Locate every blood parasite and identify its species.
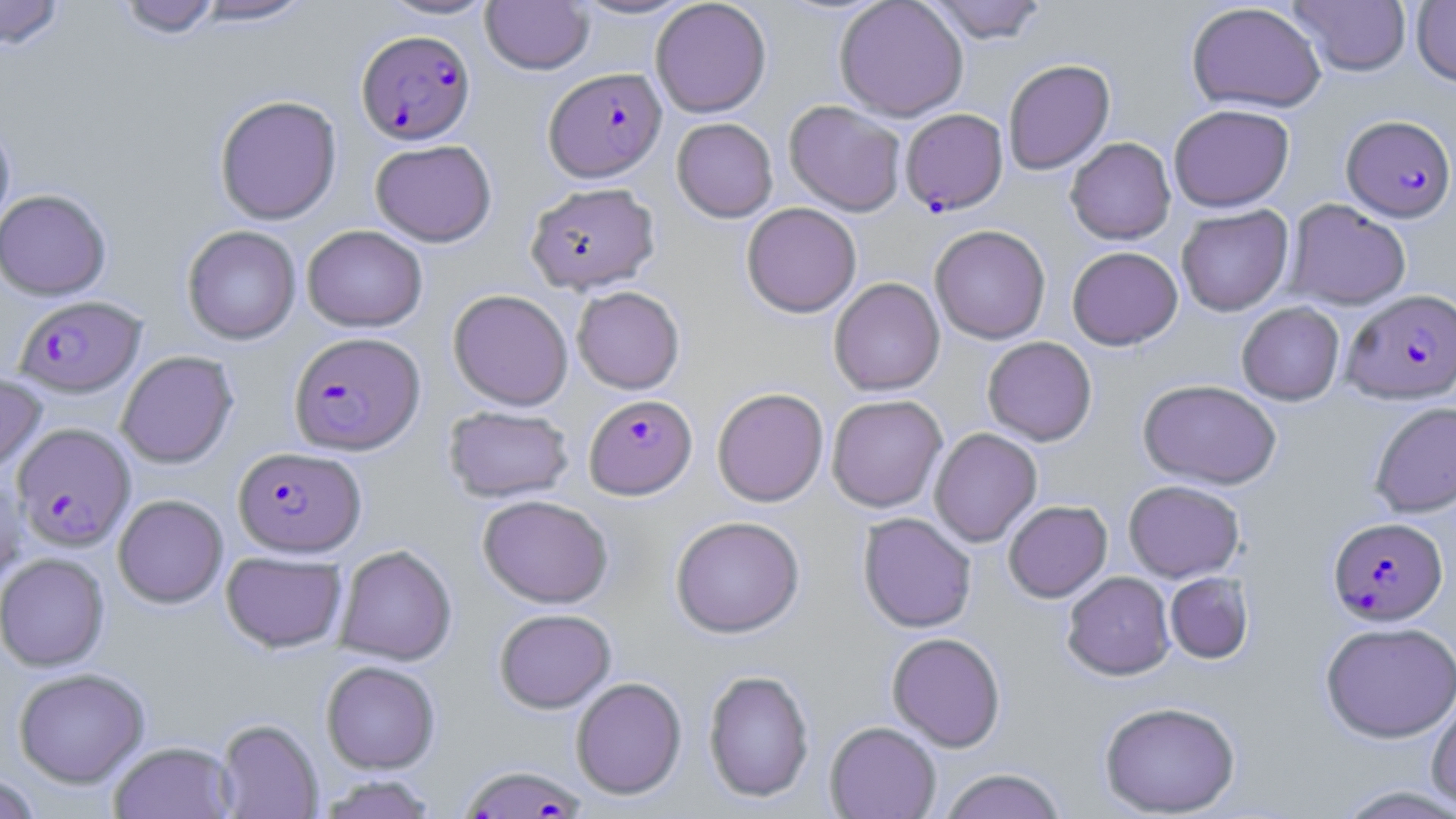
Approximate bounding boxes as named x1/y1/x2/y2 corners in pixels.
Plasmodium falciparum-infected red blood cells: (x1=356, y1=29, x2=475, y2=144), (x1=544, y1=66, x2=667, y2=182), (x1=900, y1=108, x2=1008, y2=214), (x1=1342, y1=115, x2=1455, y2=222), (x1=1342, y1=289, x2=1456, y2=404), (x1=14, y1=295, x2=146, y2=397), (x1=289, y1=331, x2=425, y2=455), (x1=584, y1=394, x2=697, y2=499), (x1=13, y1=423, x2=135, y2=551), (x1=233, y1=446, x2=366, y2=557), (x1=1328, y1=517, x2=1448, y2=625), (x1=458, y1=764, x2=587, y2=819).
No Plasmodium ovale, Plasmodium malariae, Plasmodium vivax, Babesia divergens, or Trypanosoma brucei observed.

Uninfected red blood cell locations: (x1=0, y1=0, x2=65, y2=50), (x1=115, y1=0, x2=222, y2=39), (x1=188, y1=0, x2=315, y2=26), (x1=377, y1=0, x2=499, y2=20), (x1=567, y1=0, x2=698, y2=20), (x1=650, y1=0, x2=772, y2=118), (x1=834, y1=0, x2=969, y2=121), (x1=923, y1=0, x2=1049, y2=43), (x1=1288, y1=0, x2=1412, y2=76), (x1=1411, y1=0, x2=1456, y2=87), (x1=481, y1=1, x2=594, y2=75), (x1=1186, y1=2, x2=1326, y2=114), (x1=1003, y1=58, x2=1115, y2=175), (x1=214, y1=95, x2=342, y2=225), (x1=783, y1=100, x2=906, y2=216), (x1=1168, y1=104, x2=1294, y2=212), (x1=672, y1=117, x2=778, y2=222), (x1=0, y1=121, x2=15, y2=235), (x1=1065, y1=137, x2=1176, y2=244), (x1=370, y1=139, x2=497, y2=247), (x1=525, y1=182, x2=661, y2=293), (x1=0, y1=189, x2=111, y2=300), (x1=1284, y1=199, x2=1411, y2=311), (x1=741, y1=202, x2=862, y2=318), (x1=1176, y1=205, x2=1293, y2=316), (x1=302, y1=225, x2=427, y2=332), (x1=929, y1=225, x2=1051, y2=344), (x1=182, y1=226, x2=301, y2=344), (x1=1067, y1=246, x2=1183, y2=350), (x1=829, y1=278, x2=945, y2=396), (x1=572, y1=286, x2=685, y2=394), (x1=448, y1=289, x2=573, y2=411), (x1=1236, y1=302, x2=1345, y2=405), (x1=982, y1=336, x2=1097, y2=446), (x1=116, y1=351, x2=238, y2=469), (x1=0, y1=371, x2=47, y2=475), (x1=1138, y1=379, x2=1283, y2=489), (x1=712, y1=387, x2=829, y2=507), (x1=826, y1=394, x2=947, y2=513), (x1=1370, y1=401, x2=1456, y2=518), (x1=443, y1=406, x2=574, y2=503), (x1=929, y1=428, x2=1042, y2=547), (x1=0, y1=471, x2=27, y2=592), (x1=1123, y1=480, x2=1244, y2=582), (x1=114, y1=494, x2=228, y2=608), (x1=477, y1=495, x2=613, y2=608), (x1=1003, y1=500, x2=1113, y2=602), (x1=858, y1=513, x2=977, y2=633), (x1=670, y1=516, x2=805, y2=638), (x1=335, y1=545, x2=457, y2=665), (x1=221, y1=551, x2=348, y2=653), (x1=0, y1=553, x2=109, y2=671), (x1=1062, y1=572, x2=1175, y2=680), (x1=1164, y1=572, x2=1254, y2=664), (x1=494, y1=609, x2=616, y2=713), (x1=1320, y1=621, x2=1456, y2=742), (x1=886, y1=632, x2=1006, y2=751), (x1=321, y1=661, x2=440, y2=774), (x1=12, y1=668, x2=150, y2=788), (x1=702, y1=669, x2=815, y2=803), (x1=571, y1=677, x2=687, y2=799), (x1=1427, y1=691, x2=1456, y2=811), (x1=1098, y1=701, x2=1241, y2=817), (x1=215, y1=718, x2=323, y2=818), (x1=825, y1=721, x2=941, y2=819), (x1=108, y1=741, x2=237, y2=819), (x1=938, y1=768, x2=1067, y2=819), (x1=0, y1=773, x2=43, y2=818), (x1=315, y1=774, x2=440, y2=818), (x1=1332, y1=784, x2=1456, y2=819). Slide-level diagnosis: Plasmodium falciparum. Thin blood film. May-Grünwald-Giemsa stain. One field of a larger specimen. Image is 1456×819 pixels. Optical microscopy. 1000x magnification.